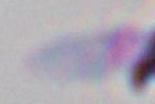

Summary:
  - Magnification: 1000x
  - Identification: Toxoplasma gondii
  - Modality: photomicrograph